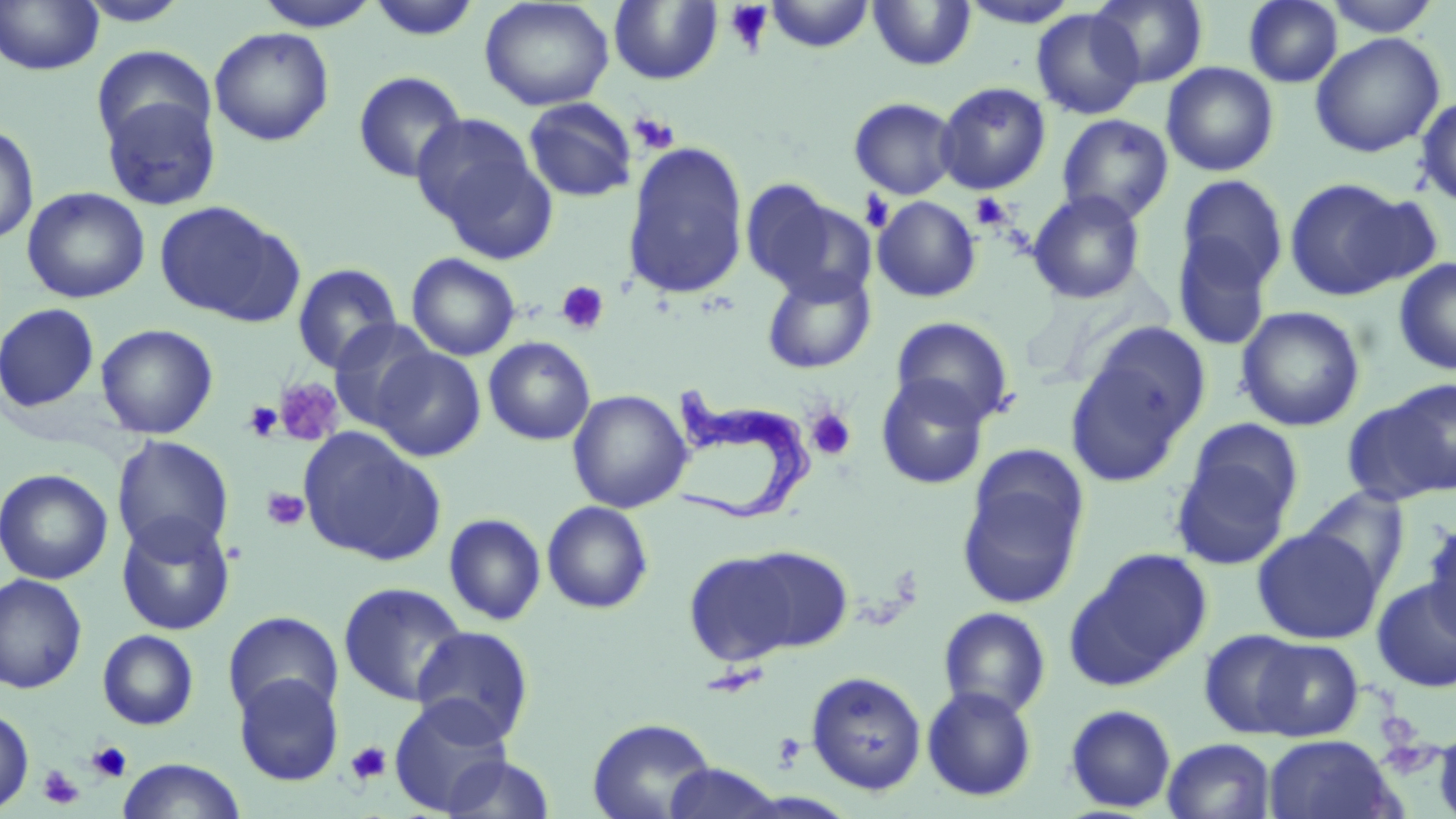

slide-level diagnosis = Trypanosoma brucei
stain = May-Grünwald-Giemsa
Trypanosoma brucei locations = approximate bounding boxes as (x1,y1)-(x2,y2) corner pairs in pixels: (662,376)-(820,526)
field of view = single
image size = 1456×819 pixels
uninfected red blood cell locations = approximate bounding boxes as (x1,y1)-(x2,y2) corner pairs in pixels: (74,0)-(194,27), (367,0)-(482,41), (479,0)-(614,112), (764,0)-(875,53), (868,0)-(976,70), (958,0)-(1082,28), (1090,0)-(1208,88), (1243,0)-(1342,88), (1323,0)-(1442,38), (0,1)-(104,76), (252,1)-(381,30), (609,1)-(722,85), (1032,7)-(1144,120), (209,26)-(334,146), (1310,32)-(1445,158), (92,46)-(215,154), (1161,62)-(1279,176), (353,71)-(468,184), (935,81)-(1051,195), (100,95)-(221,210), (1414,95)-(1456,207), (523,97)-(637,202), (849,97)-(960,200), (412,113)-(553,256), (1056,113)-(1174,224), (0,122)-(39,244), (622,142)-(749,300), (1176,174)-(1289,295), (1283,178)-(1421,301), (740,180)-(859,298), (21,187)-(150,304), (1027,190)-(1147,305), (872,196)-(981,302), (154,199)-(303,325), (1172,229)-(1276,352), (407,253)-(520,360), (1393,257)-(1456,376), (291,263)-(402,374), (761,268)-(877,375), (0,302)-(100,413), (1235,306)-(1365,432), (0,310)-(201,423), (891,316)-(1015,427), (327,319)-(441,431), (1086,321)-(1212,436), (96,323)-(218,439), (484,337)-(596,445), (1064,345)-(1200,489), (371,346)-(487,463), (875,374)-(990,491), (1376,379)-(1456,498), (568,389)-(693,513), (1184,418)-(1304,527), (299,427)-(446,565), (112,435)-(234,559), (1170,450)-(1297,571), (0,468)-(113,584), (957,469)-(1087,609), (1302,485)-(1412,595), (542,501)-(654,614), (116,513)-(236,635), (443,513)-(547,626), (1421,518)-(1456,646), (1252,527)-(1383,644), (734,545)-(854,654), (1067,549)-(1213,688), (683,550)-(808,667), (0,574)-(87,694), (1371,578)-(1456,692), (338,581)-(469,706), (938,606)-(1051,719), (223,610)-(343,720), (410,625)-(535,745), (96,629)-(200,731), (1199,629)-(1311,739), (1250,638)-(1364,741), (805,671)-(927,795), (234,672)-(343,786), (921,685)-(1038,801), (388,695)-(515,815), (1064,704)-(1176,813), (0,707)-(34,813), (586,717)-(717,819), (1435,722)-(1456,819), (1263,734)-(1400,819), (1162,737)-(1277,819), (439,754)-(556,818), (116,758)-(247,819), (659,764)-(787,819)
magnification = 1000x
modality = light microscopy
preparation = thin blood smear
platelet locations = approximate bounding boxes as (x1,y1)-(x2,y2) corner pairs in pixels: (725,1)-(774,54), (629,112)-(680,155), (859,191)-(895,233), (970,193)-(1013,232), (555,281)-(610,335), (274,377)-(344,448), (243,402)-(284,441), (805,407)-(856,461), (261,487)-(308,531), (88,741)-(132,783), (345,741)-(391,787), (38,765)-(83,809)